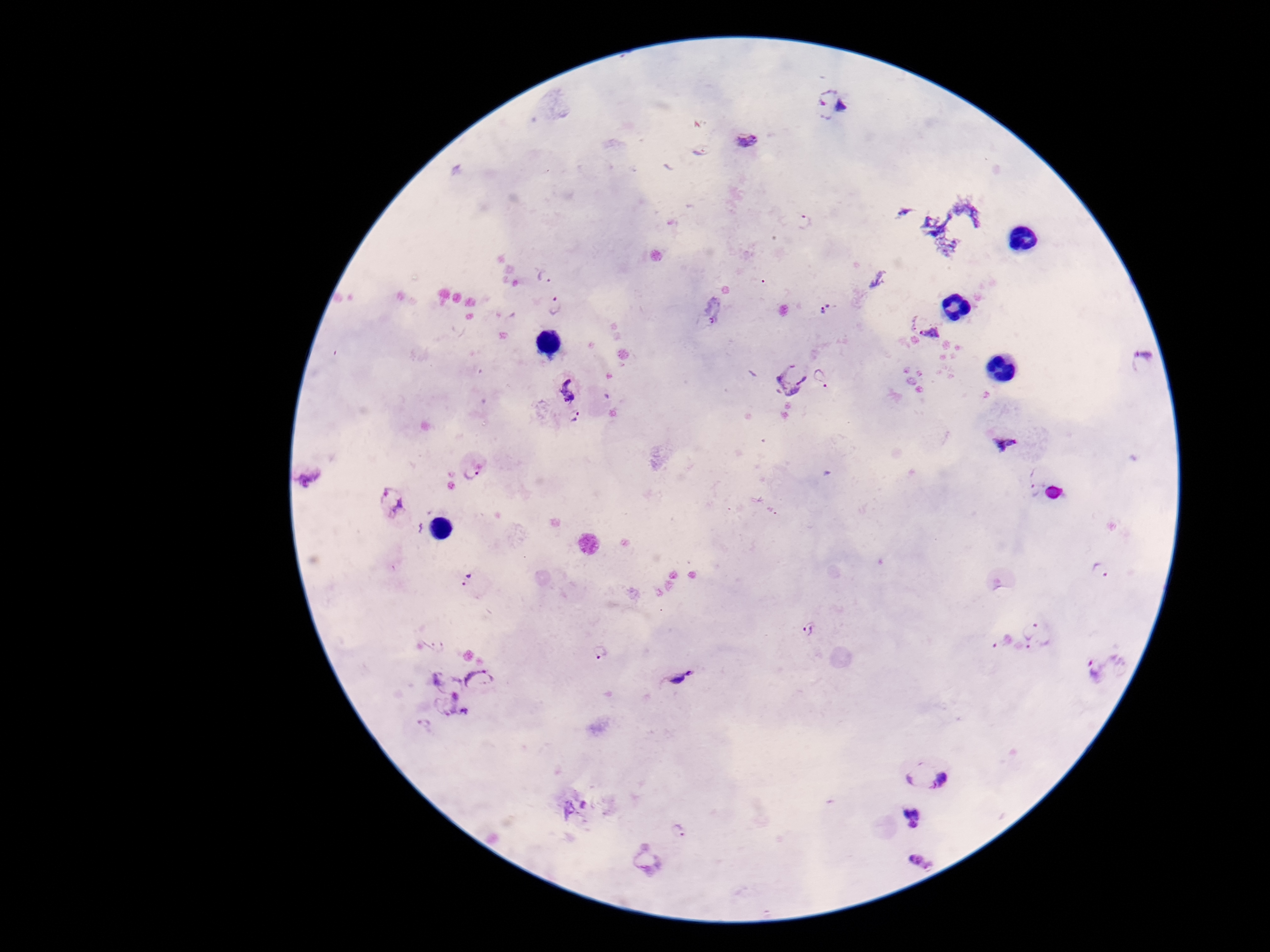
{
  "capture": "smartphone camera through the microscope eyepiece",
  "stain": "Giemsa",
  "magnification": "100x",
  "field_of_view": "single",
  "preparation": "thick blood film",
  "plasmodium_parasite_locations": "approximate object centers, in pixels from the top-left corner: (x=834, y=106), (x=746, y=141), (x=702, y=150), (x=806, y=224), (x=544, y=277), (x=555, y=306), (x=712, y=308), (x=827, y=310), (x=924, y=326), (x=1143, y=360), (x=822, y=378), (x=789, y=379), (x=567, y=390), (x=575, y=420), (x=1007, y=442), (x=473, y=471), (x=306, y=476), (x=1034, y=490), (x=392, y=503), (x=1101, y=571), (x=467, y=580), (x=811, y=630), (x=1037, y=634), (x=1003, y=640), (x=435, y=643), (x=602, y=652), (x=1107, y=664), (x=679, y=677), (x=447, y=679), (x=481, y=682), (x=453, y=713), (x=421, y=728), (x=927, y=770), (x=911, y=817), (x=679, y=827), (x=648, y=861), (x=921, y=863)",
  "image_size": "1270×952 pixels",
  "patient_malaria_status": "infected"
}